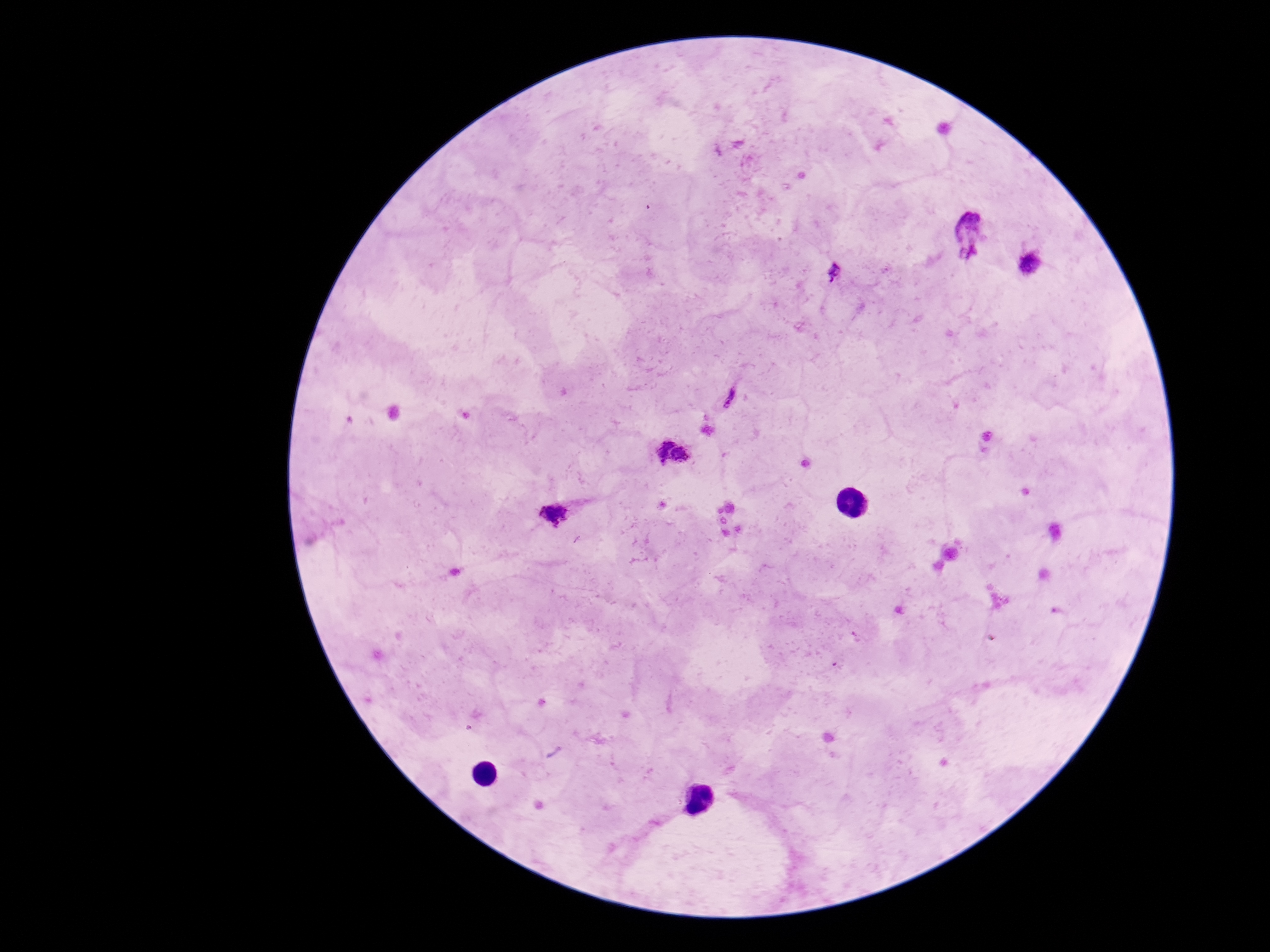

Approximate object centers, in pixels from the top-left corner. Plasmodium parasite locations: (x=972, y=230), (x=1031, y=262), (x=833, y=272), (x=730, y=397), (x=672, y=450), (x=556, y=514). Thick blood film. 100x magnification. Image is 1270×952 pixels. One field from this slide. Patient malaria status: infected. Giemsa-stained preparation. Photographed through the microscope eyepiece with a smartphone camera.